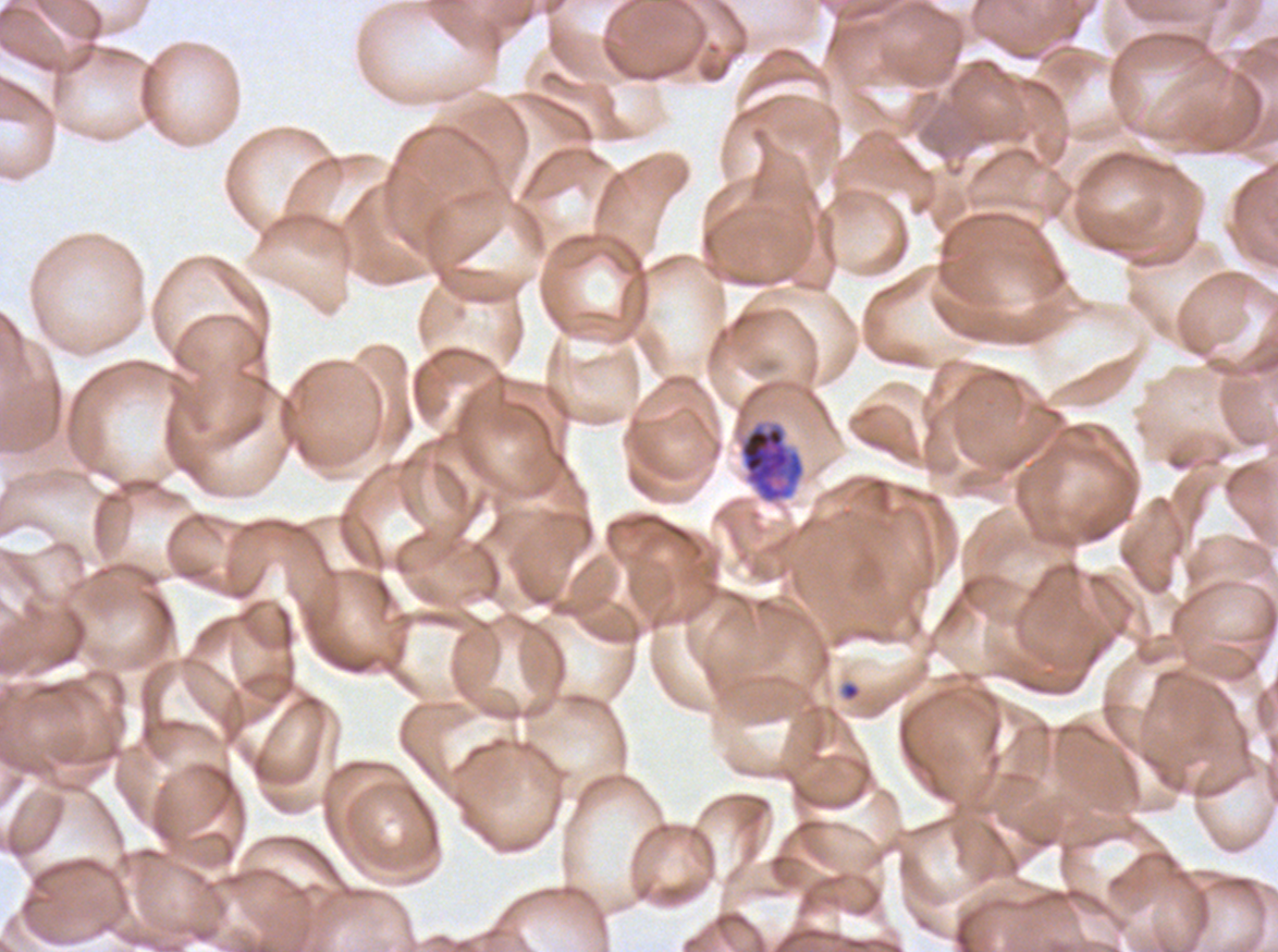
Approximate bounding boxes as [x1, y1, x2, y2] in pixels. Ring locations: [842, 682, 860, 701]. Early schizont locations: [738, 420, 806, 505]. One sub-image of a larger composite. Thin blood smear. Image is 1278×952 pixels. Life-cycle stages observed: ring, early schizont. Giemsa-stained preparation. Ex-vivo Plasmodium falciparum culture from a patient in The Gambia, grown for 24 to 48 hours.